Locate every malaria parasite and every leukocyte.
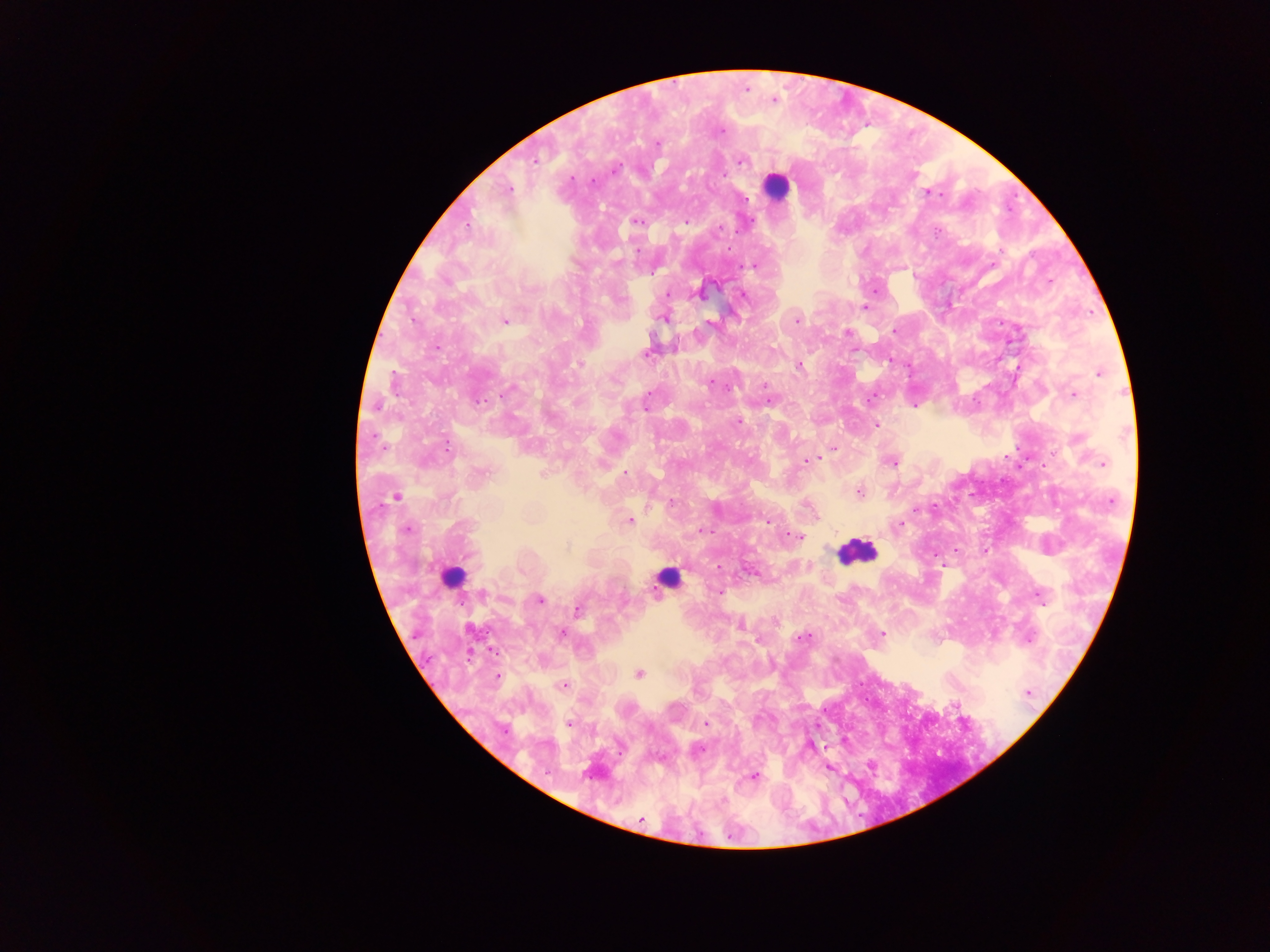

Approximate centers as [x, y] in pixels.
Malaria parasites: [773, 101], [720, 132], [742, 161], [616, 167], [688, 177], [910, 177], [929, 194], [635, 220], [686, 221], [939, 232], [753, 267], [1051, 281], [699, 293], [743, 295], [863, 306], [945, 309], [664, 314], [797, 319], [710, 320], [504, 322], [892, 330], [846, 332], [439, 346], [647, 353], [887, 361], [578, 365], [797, 366], [1101, 372], [395, 383], [767, 384], [708, 385], [510, 388], [731, 388], [1073, 393], [739, 422], [876, 425], [837, 448], [814, 460], [804, 461], [891, 463], [1103, 463], [544, 473], [626, 476], [859, 492], [396, 495], [629, 521], [766, 521], [408, 528], [794, 536], [567, 546], [719, 590], [540, 599], [577, 610], [740, 627], [561, 632], [882, 633], [807, 637], [800, 638], [639, 673], [495, 678], [564, 686], [953, 706], [759, 720], [567, 723], [705, 724], [811, 748], [697, 750], [869, 764], [829, 767], [754, 778], [639, 820].
Leukocytes: [777, 187], [852, 554], [669, 579], [453, 581].

Summary:
  - Preparation: thick blood film
  - Country: Ghana
  - Image size: 1270×952 pixels
  - Field of view: single
  - Capture: mobile-phone photograph through a microscope